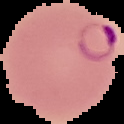
{
  "image_size": "124×124 pixels",
  "preparation": "thin blood film",
  "malaria_status": "parasitized",
  "image_type": "cell region segmented out of the field of view; surrounding area masked to black"
}